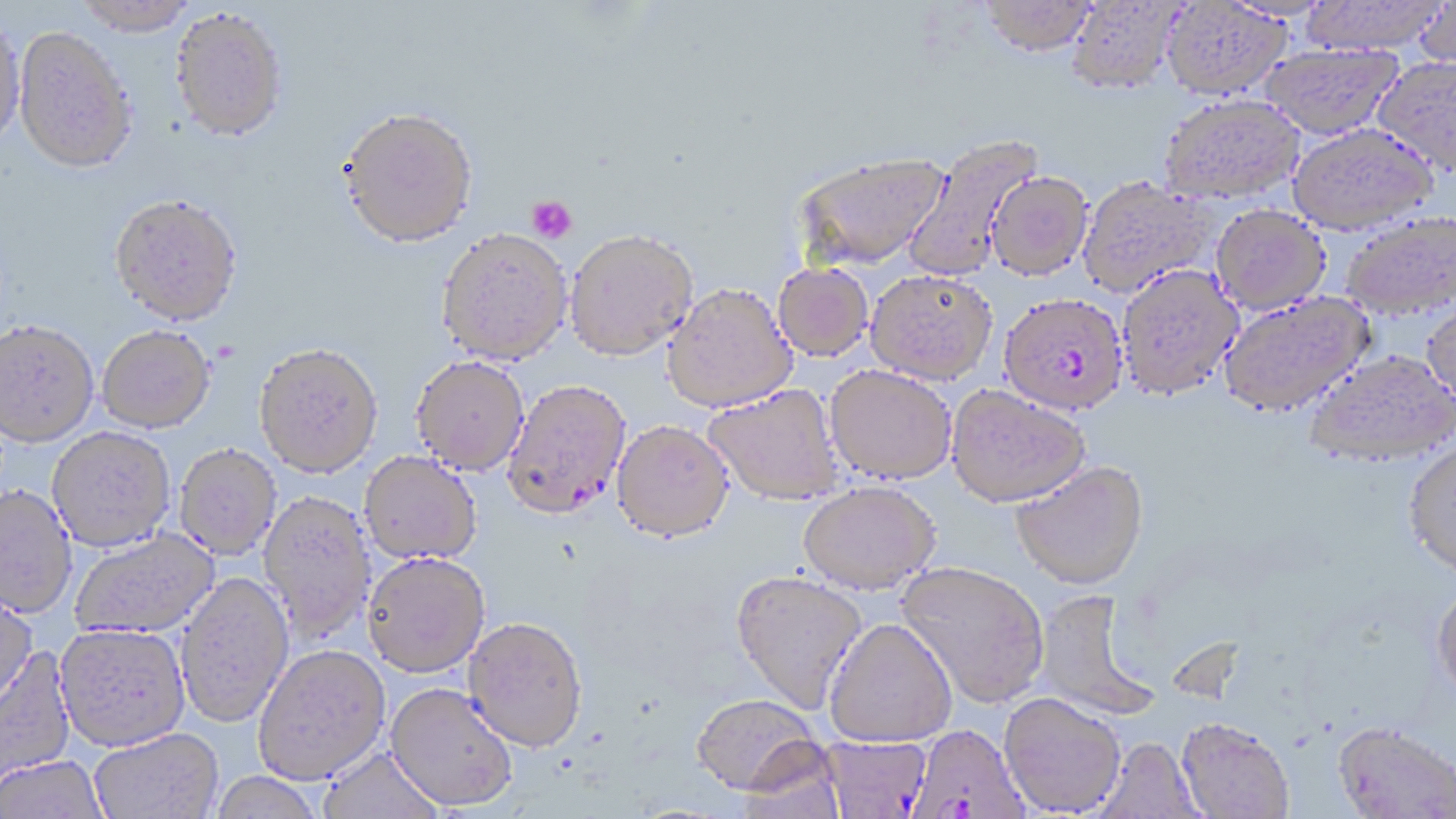
slide-level diagnosis = Plasmodium falciparum
uninfected red blood cell locations = approximate bounding boxes as (x1,y1)-(x2,y2) corner pairs in pixels: (1299,0)-(1449,54), (70,1)-(200,40), (979,1)-(1096,56), (1066,1)-(1186,95), (1412,1)-(1456,71), (1162,2)-(1291,99), (169,12)-(288,146), (0,23)-(26,155), (13,30)-(137,179), (1259,43)-(1401,139), (1373,56)-(1456,174), (1158,94)-(1305,204), (337,112)-(479,253), (1287,122)-(1439,234), (903,133)-(1043,281), (794,151)-(949,270), (986,169)-(1093,280), (1077,176)-(1217,298), (108,198)-(244,331), (1210,204)-(1331,315), (1340,211)-(1456,320), (564,231)-(698,363), (436,232)-(573,369), (772,262)-(874,362), (1115,263)-(1243,401), (866,269)-(997,384), (662,284)-(798,413), (1219,291)-(1376,418), (1421,299)-(1456,415), (0,324)-(98,451), (97,329)-(215,436), (253,347)-(383,482), (1303,348)-(1454,466), (410,359)-(529,478), (825,365)-(957,485), (704,383)-(845,506), (946,384)-(1091,508), (611,421)-(735,544), (47,430)-(176,555), (1403,439)-(1456,576), (175,446)-(281,561), (359,454)-(481,567), (1011,460)-(1149,589), (797,481)-(941,595), (0,487)-(77,621), (257,492)-(376,645), (71,530)-(221,640), (362,556)-(491,681), (895,561)-(1049,708), (730,569)-(868,713), (174,573)-(294,731), (1430,584)-(1456,704), (0,588)-(39,715), (1033,589)-(1161,722), (824,618)-(958,746), (462,620)-(588,756), (54,626)-(190,754), (0,647)-(77,791), (253,647)-(391,787), (384,685)-(518,814), (999,693)-(1126,816), (690,694)-(825,796), (1176,717)-(1295,818), (1332,725)-(1456,818), (90,729)-(224,819), (821,736)-(932,818), (1095,738)-(1204,819), (736,741)-(847,818), (318,747)-(443,818), (0,757)-(109,819), (208,773)-(325,819)
stain = May-Grünwald-Giemsa
modality = optical microscopy
field of view = one of a larger specimen
magnification = 1000x
preparation = thin blood film
platelet locations = approximate bounding boxes as (x1,y1)-(x2,y2) corner pairs in pixels: (526,195)-(577,244)
image size = 1456×819 pixels
Plasmodium falciparum-infected red blood cell locations = approximate bounding boxes as (x1,y1)-(x2,y2) corner pairs in pixels: (999,298)-(1125,419), (502,382)-(632,523), (905,724)-(1030,819)